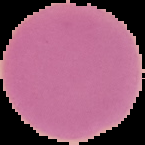

result: no malaria parasites detected
image_size: 145×145 pixels
image_type: segmented cell region with the area outside set to black
preparation: thin blood film